Name the parasite shown.
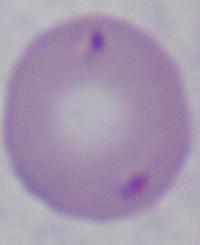

This is Babesia.

magnification = 1000x
modality = micrograph